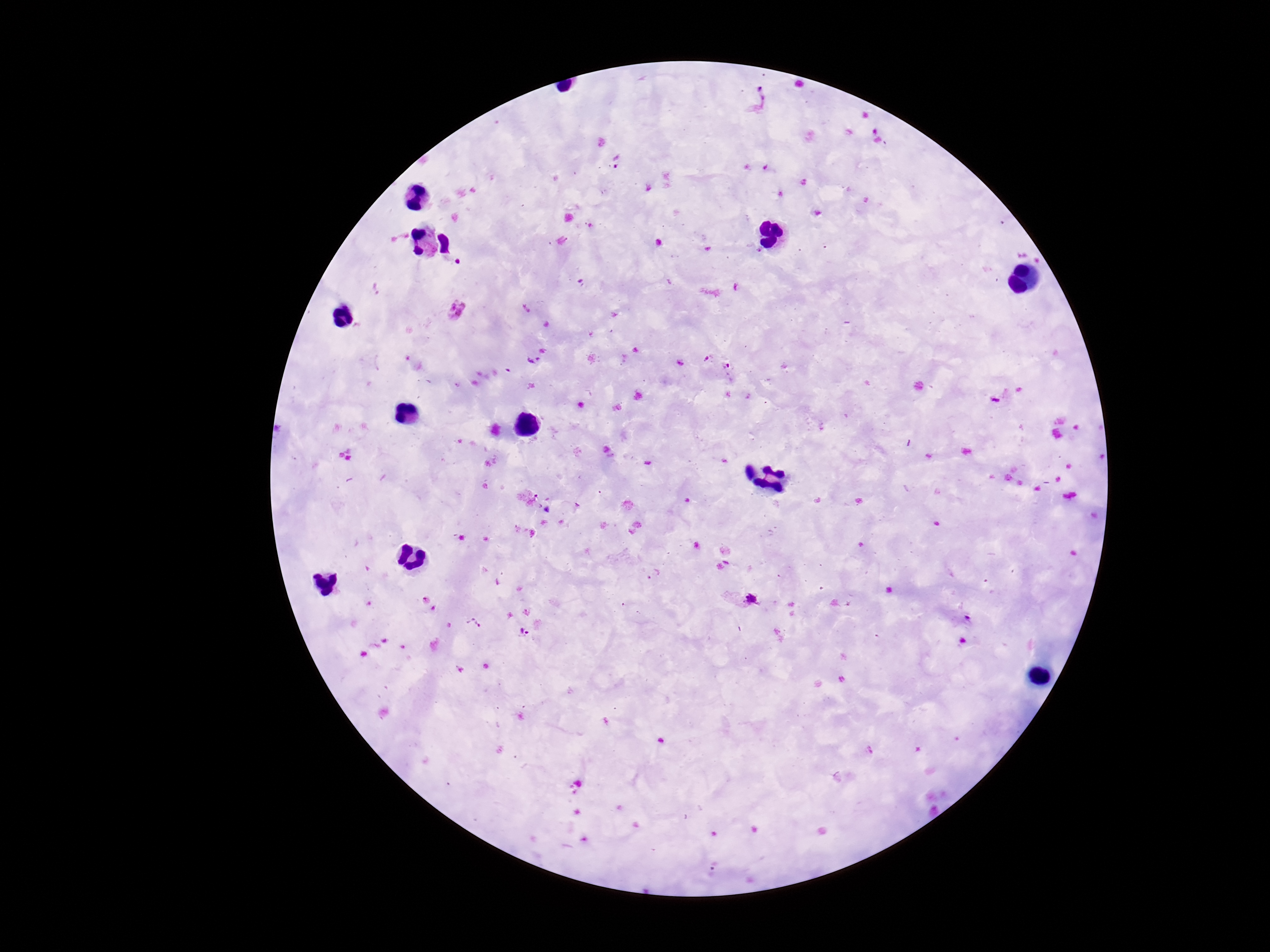

image size = 1270×952 pixels
capture = smartphone camera through the microscope eyepiece
preparation = thick blood film
magnification = 100x
patient malaria status = infected
Plasmodium parasite locations = approximate centers as (x, y) in pixels: (758, 103), (614, 162), (456, 310), (705, 356), (531, 359), (729, 369), (653, 574), (741, 598), (472, 623), (523, 631), (717, 865)
field of view = single
stain = Giemsa